Report the malaria status of this cell.
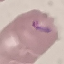
It is parasitized.

Summary:
  - Preparation: thin blood smear
  - Image type: cell patch, automatically extracted from a larger field of view and resized to 64 × 64 pixels
  - Stain: Giemsa
  - Capture: smartphone through the microscope eyepiece